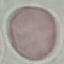 Malaria status: uninfected. Thin blood film. Cell patch, automatically extracted from a larger field of view and resized to 64 × 64 pixels. Acquired by smartphone through the microscope eyepiece. Giemsa-stained preparation.